State the preparation type.
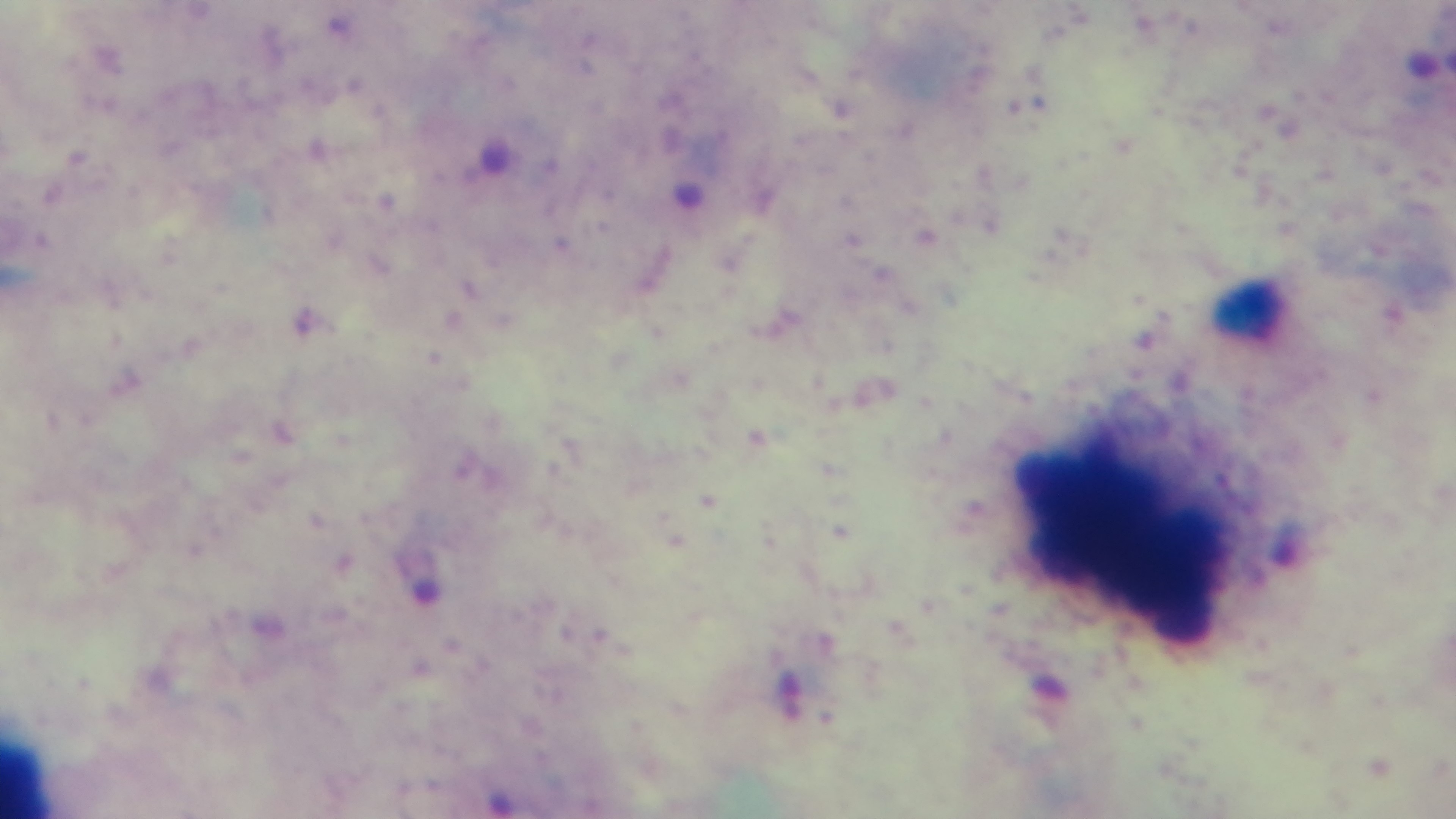
Thick.

Summary:
  - Field of view: single
  - Objective: 100x oil immersion
  - Capture: mounted 4K digital camera
  - Stain: Giemsa
  - Modality: light microscopy
  - Malaria status: positive